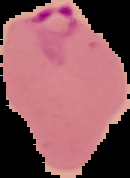
Summary:
  - Preparation: thin blood film
  - Image type: cell region segmented out of the field of view; surrounding area masked to black
  - Result: Plasmodium parasites detected
  - Image size: 130×178 pixels